Name the parasite shown.
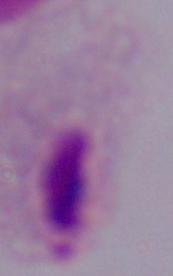

This is a trichomonad.

modality: micrograph
magnification: 1000x